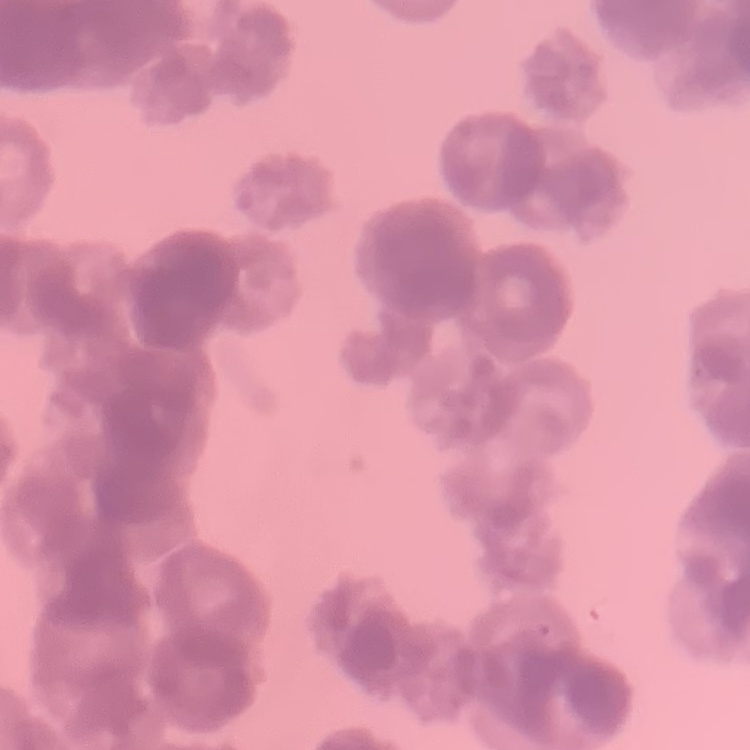
Summary:
  - Erythrocyte morphology: rouleaux formation
  - Image type: one tile cut from a larger photomicrograph
  - Preparation: thin blood smear
  - Stain: Field's or Giemsa